Give the position of every Plasmodium parasite, noting whether each is a trophozoite, schizont, or gametocyte.
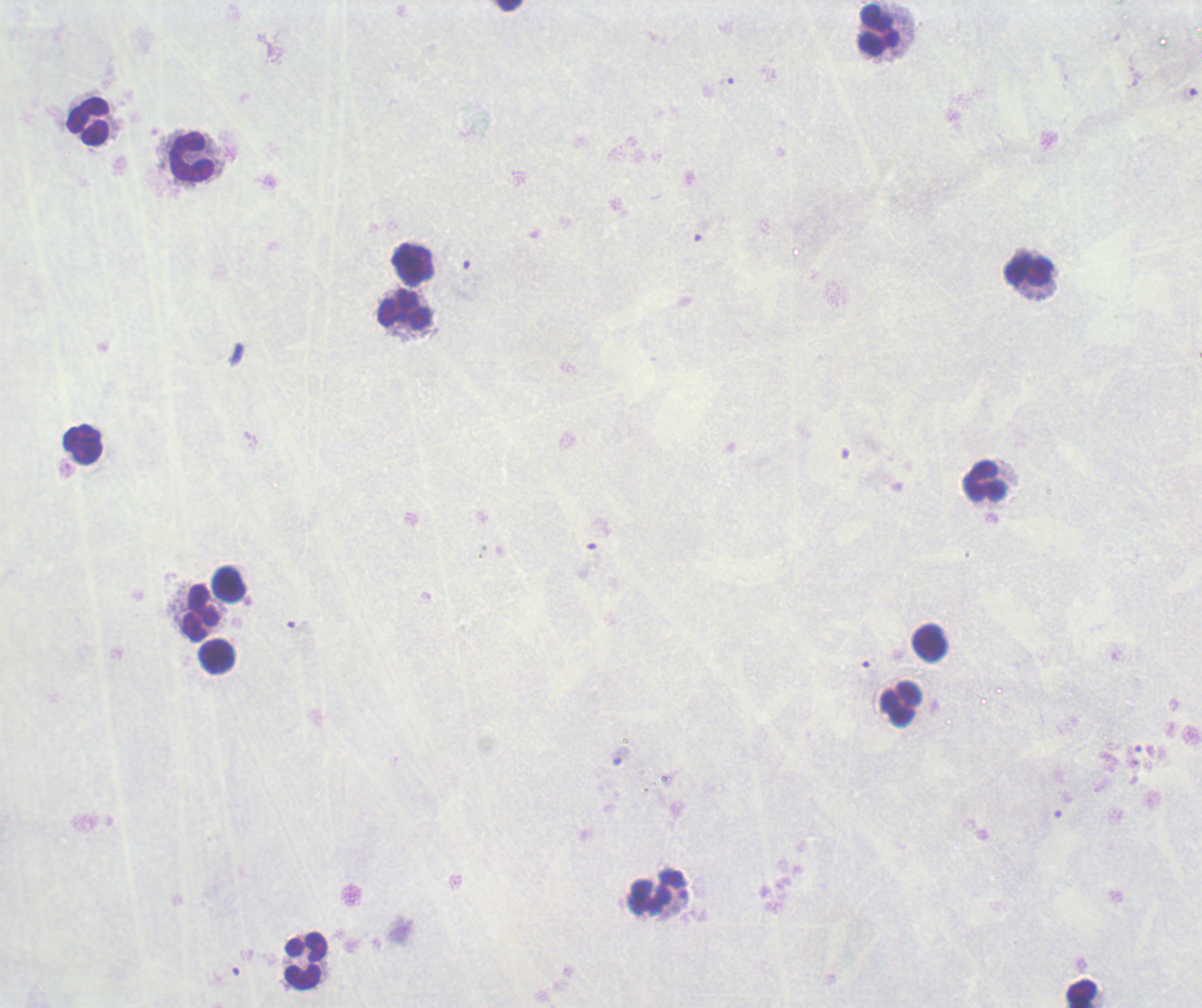

No Plasmodium parasites seen.

Approximate centers as (x, y) in pixels.
Summary:
  - Leukocyte locations: (880, 31), (89, 122), (192, 157), (1030, 272), (405, 310), (84, 445), (986, 482), (230, 586), (201, 613), (930, 643), (216, 656), (901, 705), (657, 892), (305, 960), (1083, 995)
  - Field of view: single
  - Preparation: thick smear of blood
  - Stain: Romanowsky
  - Background quality: unsatisfactory
  - Magnification: 100x
  - Image size: 1202×1008 pixels
  - Context: previously used in an actual diagnosis